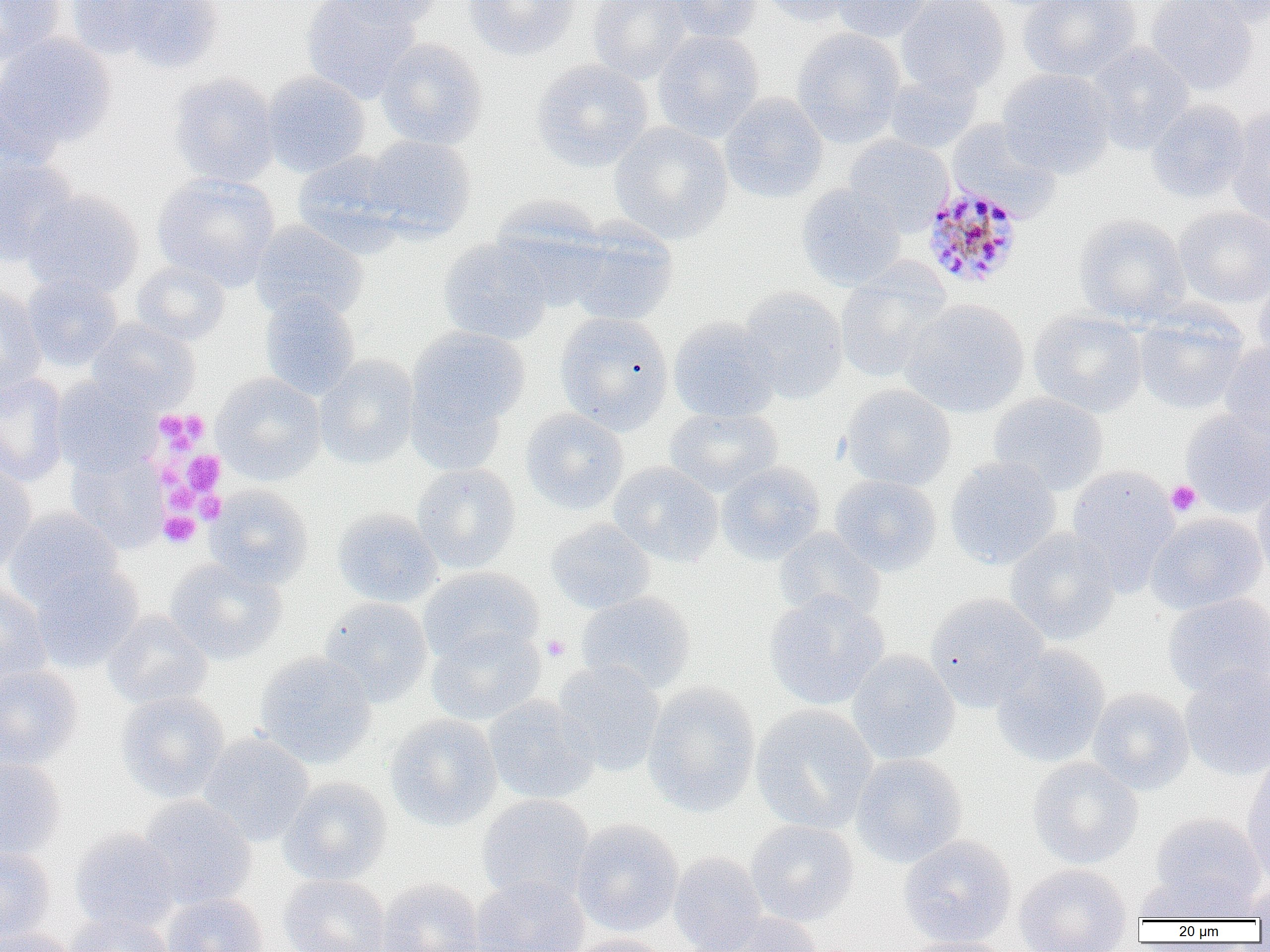

Plasmodium malariae-infected red blood cell locations = approximate bounding boxes as (x1,y1)-(x2,y2) corner pairs in pixels: (920,185)-(1025,290)
slide-level diagnosis = Plasmodium malariae
image size = 1270×952 pixels
field of view = one of a larger specimen
uninfected red blood cell locations = approximate bounding boxes as (x1,y1)-(x2,y2) corner pairs in pixels: (0,0)-(64,65), (66,0)-(177,61), (301,0)-(421,101), (326,0)-(441,28), (463,0)-(582,62), (587,0)-(693,83), (667,0)-(761,44), (759,0)-(860,26), (830,0)-(936,43), (896,0)-(1010,96), (1017,0)-(1141,82), (1145,0)-(1260,95), (1179,0)-(1270,30), (98,1)-(225,71), (792,28)-(906,147), (652,30)-(764,143), (0,33)-(116,157), (375,37)-(488,150), (1085,43)-(1194,153), (532,59)-(653,172), (996,68)-(1116,178), (882,70)-(982,154), (262,72)-(370,177), (168,73)-(280,188), (720,93)-(827,204), (1145,99)-(1251,203), (1227,107)-(1270,226), (946,119)-(1061,219), (608,122)-(733,243), (362,135)-(477,239), (843,136)-(953,233), (292,151)-(406,255), (0,154)-(79,266), (152,173)-(280,291), (796,185)-(906,290), (23,189)-(145,299), (489,198)-(610,309), (1173,206)-(1270,307), (1073,214)-(1192,325), (562,219)-(679,325), (250,220)-(369,324), (437,238)-(554,344), (131,260)-(231,345), (834,267)-(950,384), (21,274)-(123,372), (1252,277)-(1270,372), (0,287)-(47,396), (737,287)-(848,403), (259,292)-(360,399), (901,298)-(1029,419), (1133,305)-(1249,415), (1028,308)-(1148,417), (554,311)-(675,434), (668,317)-(783,422), (86,319)-(200,413), (407,327)-(529,439), (1219,343)-(1270,447), (314,355)-(419,470), (211,372)-(326,484), (0,373)-(70,487), (51,377)-(157,477), (840,384)-(956,491), (989,393)-(1108,495), (664,405)-(783,497), (520,408)-(629,515), (1180,408)-(1270,518), (66,450)-(167,553), (944,457)-(1062,570), (716,461)-(826,564), (0,462)-(38,574), (609,462)-(723,566), (412,463)-(521,574), (1065,465)-(1180,590), (830,475)-(942,575), (1252,479)-(1270,581), (204,485)-(313,589), (4,508)-(124,611), (332,508)-(442,607), (1146,512)-(1267,615), (546,519)-(656,615), (773,528)-(886,624), (1004,528)-(1121,645), (166,558)-(286,664), (30,565)-(143,673), (418,567)-(544,667), (0,583)-(52,688), (765,591)-(888,711), (576,592)-(695,694), (924,593)-(1049,712), (1162,593)-(1270,699), (318,597)-(433,707), (102,611)-(213,710), (426,625)-(546,725), (990,644)-(1111,768), (847,649)-(960,766), (255,652)-(377,769), (552,660)-(665,776), (0,666)-(83,770), (1180,666)-(1270,782), (642,682)-(761,817), (1086,687)-(1195,795), (114,691)-(230,804), (484,695)-(601,804), (751,705)-(878,834), (384,714)-(503,832), (198,732)-(314,846), (850,753)-(969,867), (0,757)-(66,858), (1027,757)-(1143,869), (1242,758)-(1270,883), (278,777)-(392,886), (476,794)-(595,905), (134,796)-(257,910), (1149,813)-(1267,911), (570,818)-(684,936), (745,819)-(859,926), (69,828)-(181,934), (898,834)-(1017,948), (0,845)-(56,943), (669,851)-(767,952), (1014,863)-(1133,952), (1136,871)-(1259,923), (278,874)-(391,952), (470,876)-(590,952), (376,877)-(484,952), (1247,877)-(1270,923), (162,893)-(269,952), (708,912)-(824,951), (65,913)-(175,952), (0,927)-(75,952), (565,933)-(674,952), (896,935)-(1017,952)
modality = light microscopy
magnification = 1000x
platelet locations = approximate bounding boxes as (x1,y1)-(x2,y2) corner pairs in pixels: (156,409)-(209,451), (184,451)-(224,494), (1166,480)-(1202,516), (165,482)-(198,512), (195,491)-(225,523), (158,511)-(200,548), (541,635)-(570,661)
preparation = thin blood smear